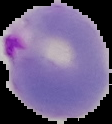

Malaria status: parasitized. From a thin blood smear. Cell region segmented out of the field of view; the surrounding area is masked to black. Image is 112×124 pixels.